Classify this cell by malaria status.
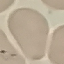

Parasitized.

Summary:
  - Image type: cell patch, automatically extracted from a larger field of view and resized to 64 × 64 pixels
  - Stain: Giemsa
  - Capture: smartphone through the microscope eyepiece
  - Preparation: thin blood film